Outline each white blood cell.
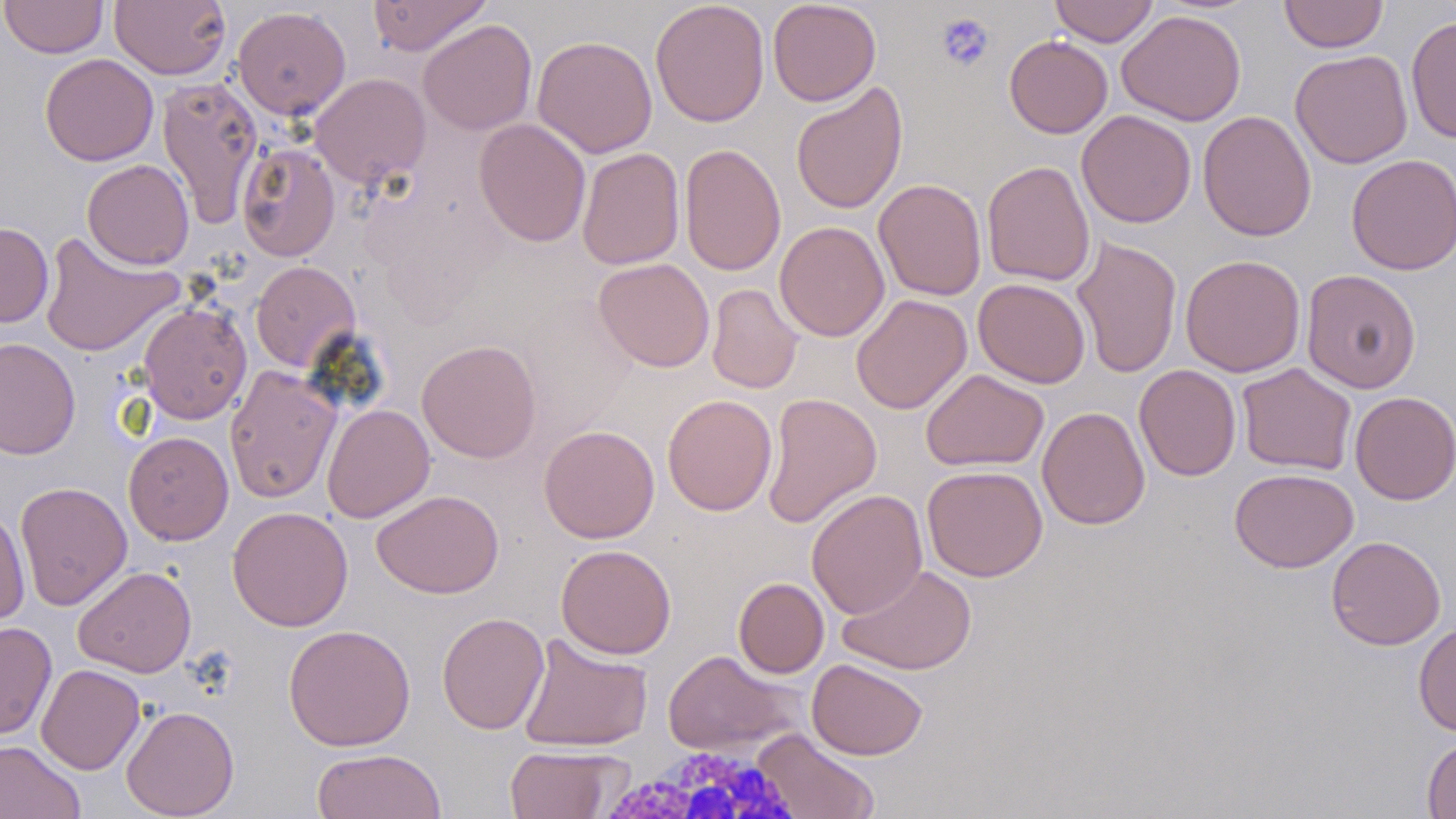

Approximate bounding boxes as named x1/y1/x2/y2 corners in pixels.
White blood cells: (x1=593, y1=743, x2=813, y2=819).

Uninfected red blood cell locations: (x1=1, y1=0, x2=108, y2=58), (x1=109, y1=0, x2=231, y2=80), (x1=366, y1=0, x2=492, y2=56), (x1=650, y1=0, x2=770, y2=127), (x1=767, y1=0, x2=882, y2=106), (x1=1049, y1=0, x2=1158, y2=46), (x1=1278, y1=0, x2=1389, y2=53), (x1=232, y1=6, x2=351, y2=120), (x1=1118, y1=9, x2=1247, y2=126), (x1=1405, y1=15, x2=1456, y2=144), (x1=417, y1=19, x2=537, y2=135), (x1=532, y1=35, x2=658, y2=159), (x1=1004, y1=35, x2=1113, y2=138), (x1=1290, y1=50, x2=1413, y2=168), (x1=40, y1=53, x2=158, y2=166), (x1=309, y1=73, x2=431, y2=189), (x1=157, y1=75, x2=263, y2=229), (x1=790, y1=81, x2=908, y2=215), (x1=1077, y1=109, x2=1196, y2=228), (x1=1198, y1=110, x2=1317, y2=241), (x1=474, y1=119, x2=592, y2=247), (x1=236, y1=142, x2=340, y2=262), (x1=679, y1=143, x2=786, y2=276), (x1=577, y1=147, x2=685, y2=270), (x1=1346, y1=154, x2=1456, y2=275), (x1=82, y1=159, x2=194, y2=269), (x1=982, y1=160, x2=1096, y2=287), (x1=873, y1=178, x2=987, y2=300), (x1=774, y1=221, x2=890, y2=342), (x1=0, y1=222, x2=53, y2=327), (x1=38, y1=231, x2=185, y2=358), (x1=1071, y1=236, x2=1183, y2=378), (x1=1180, y1=255, x2=1306, y2=377), (x1=593, y1=258, x2=715, y2=372), (x1=250, y1=260, x2=361, y2=372), (x1=1301, y1=269, x2=1422, y2=394), (x1=973, y1=278, x2=1091, y2=388), (x1=707, y1=284, x2=803, y2=393), (x1=851, y1=294, x2=972, y2=414), (x1=137, y1=301, x2=252, y2=424), (x1=0, y1=337, x2=80, y2=460), (x1=416, y1=339, x2=542, y2=463), (x1=1236, y1=363, x2=1357, y2=476), (x1=1134, y1=364, x2=1241, y2=481), (x1=225, y1=366, x2=341, y2=504), (x1=921, y1=368, x2=1049, y2=472), (x1=1350, y1=391, x2=1456, y2=505), (x1=761, y1=392, x2=882, y2=529), (x1=662, y1=395, x2=777, y2=516), (x1=322, y1=404, x2=435, y2=523), (x1=1037, y1=406, x2=1150, y2=530), (x1=539, y1=425, x2=660, y2=543), (x1=124, y1=431, x2=233, y2=545), (x1=922, y1=465, x2=1047, y2=581), (x1=1230, y1=467, x2=1357, y2=572), (x1=14, y1=481, x2=132, y2=611), (x1=371, y1=489, x2=504, y2=599), (x1=807, y1=489, x2=928, y2=619), (x1=0, y1=505, x2=30, y2=626), (x1=227, y1=506, x2=353, y2=632), (x1=1326, y1=535, x2=1446, y2=650), (x1=555, y1=544, x2=677, y2=659), (x1=838, y1=564, x2=977, y2=675), (x1=73, y1=566, x2=196, y2=678), (x1=733, y1=577, x2=829, y2=678), (x1=436, y1=612, x2=550, y2=735), (x1=0, y1=621, x2=56, y2=741), (x1=1414, y1=622, x2=1456, y2=738), (x1=283, y1=624, x2=415, y2=751), (x1=517, y1=634, x2=653, y2=752), (x1=662, y1=649, x2=806, y2=757), (x1=807, y1=658, x2=928, y2=760), (x1=36, y1=664, x2=145, y2=775), (x1=121, y1=705, x2=239, y2=818), (x1=752, y1=729, x2=879, y2=819), (x1=1422, y1=737, x2=1456, y2=819), (x1=0, y1=740, x2=85, y2=819), (x1=503, y1=745, x2=627, y2=819), (x1=311, y1=748, x2=447, y2=819). Platelet locations: (x1=936, y1=13, x2=994, y2=72). Slide-level diagnosis: negative for blood parasites. Captured at 1000x magnification. Thin blood film. Light microscopy. May-Grünwald-Giemsa-stained preparation. Single field of view. Image is 1456×819 pixels.